Assess the morphology of the erythrocytes.
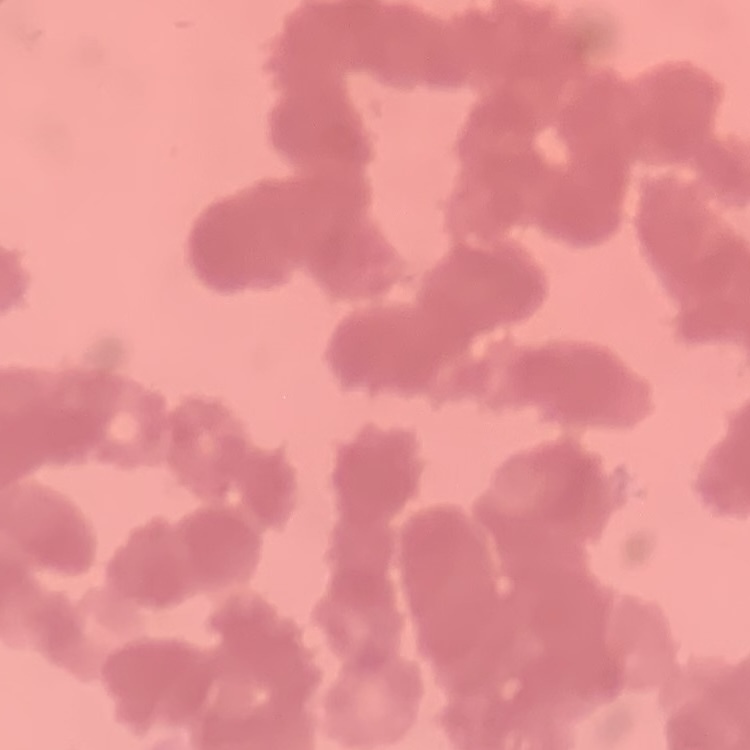
They show rouleaux formation.

stain = Field's or Giemsa
image type = square crop of a larger photomicrograph
preparation = thin peripheral smear